Locate every leukocyte (white blood cell).
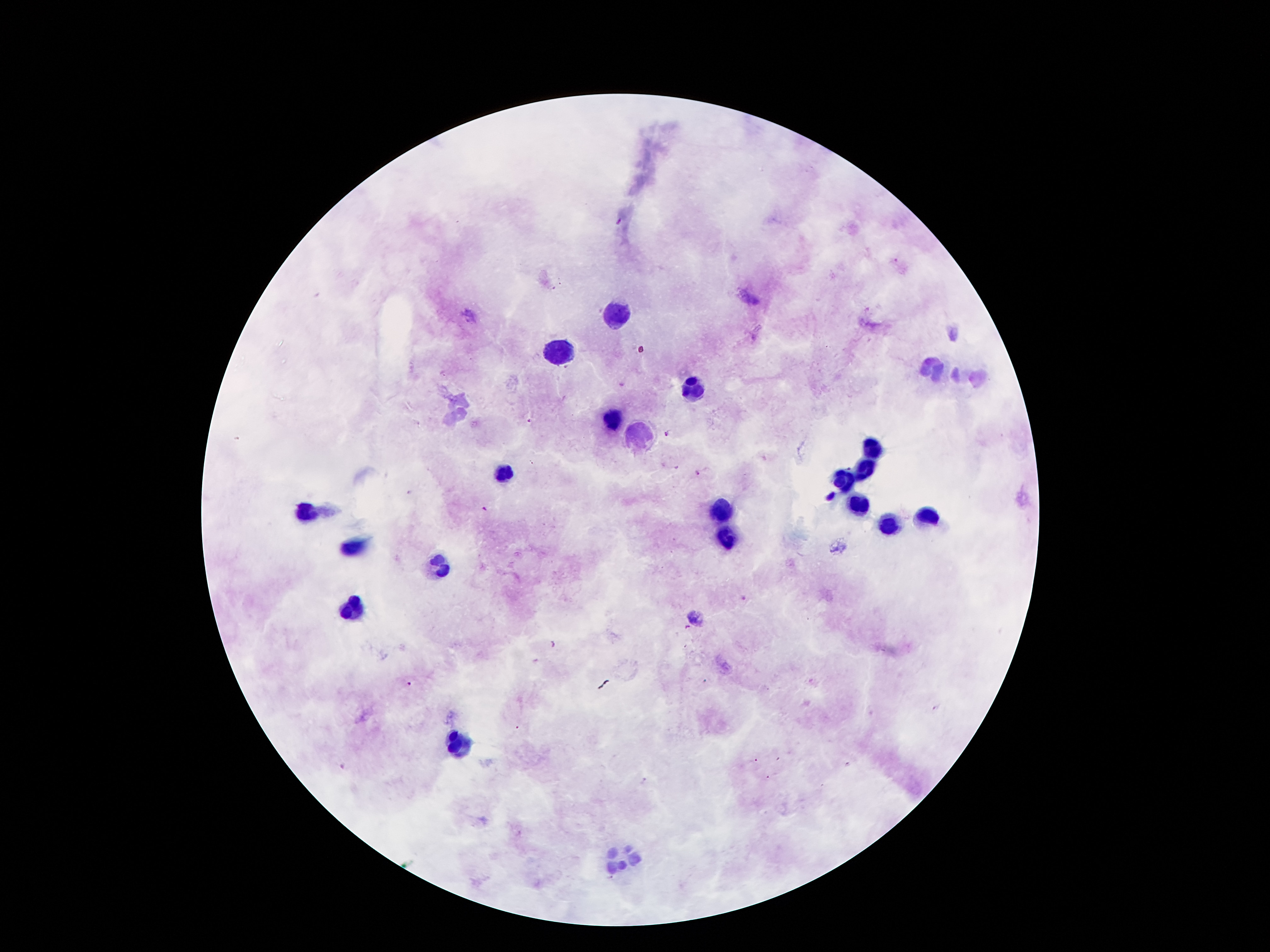

Approximate object centers, in pixels from the top-left corner.
Leukocytes: (x=615, y=314), (x=556, y=351), (x=936, y=369), (x=971, y=374), (x=694, y=387), (x=460, y=407), (x=617, y=418), (x=643, y=431), (x=873, y=449), (x=864, y=469), (x=505, y=474), (x=844, y=481), (x=855, y=504), (x=305, y=512), (x=724, y=512), (x=929, y=515), (x=887, y=525), (x=727, y=540), (x=351, y=545), (x=440, y=563), (x=356, y=604), (x=460, y=743), (x=620, y=854).

Plasmodium parasite locations: (x=527, y=422), (x=668, y=434), (x=700, y=472), (x=484, y=510), (x=743, y=597), (x=687, y=628), (x=550, y=644), (x=409, y=685), (x=936, y=708), (x=756, y=760), (x=849, y=765), (x=645, y=782), (x=609, y=878). Giemsa stain. 100x magnification. Single field of view. Thick peripheral-blood smear. Image is 1270×952 pixels. Smartphone photograph taken through the microscope eyepiece. Patient malaria status: infected with Plasmodium falciparum.